Outline each Plasmodium falciparum-infected red blood cell.
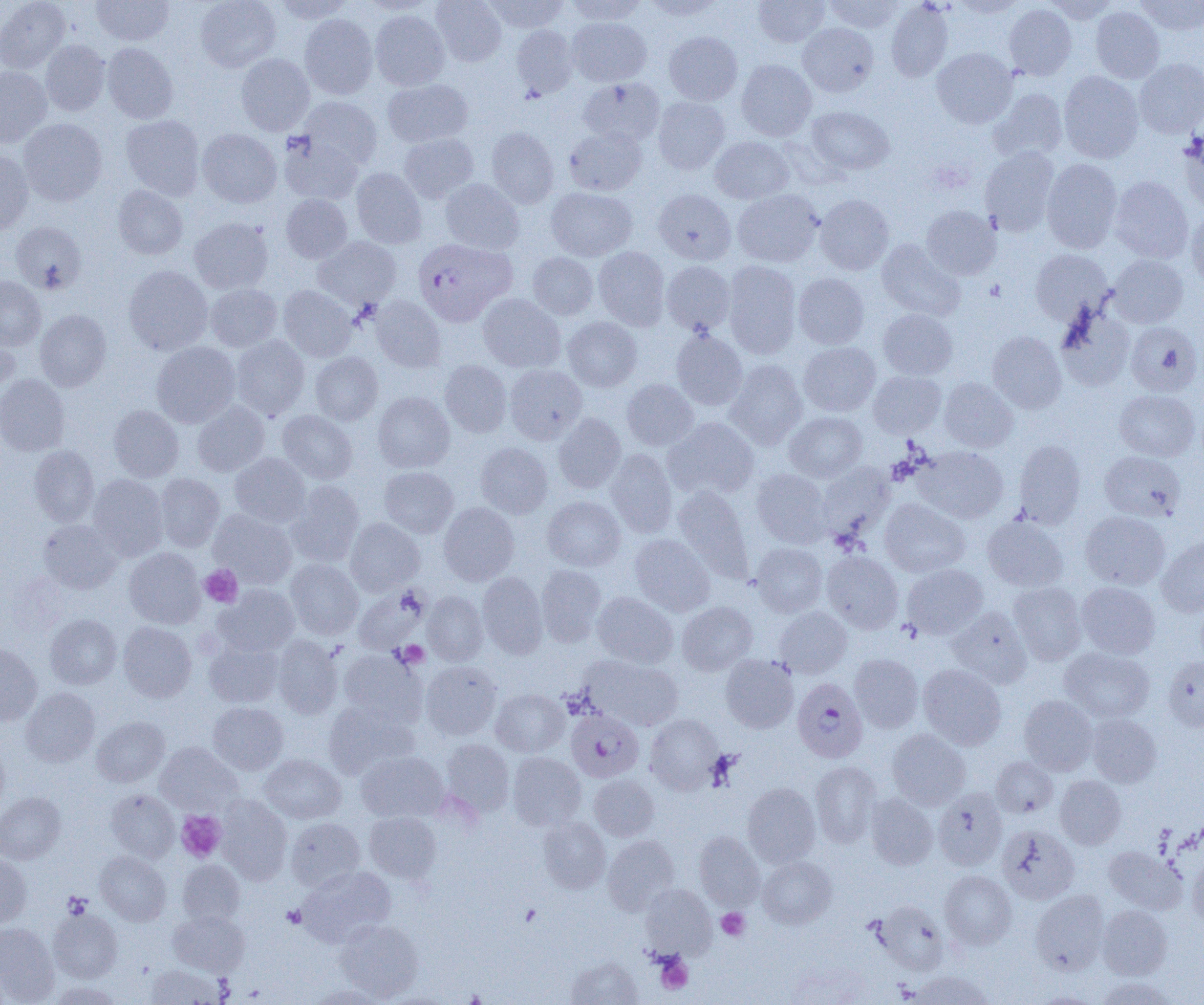

Approximate bounding boxes as [x1, y1, x2, y2] in pixels.
Plasmodium falciparum-infected red blood cells: [413, 238, 515, 326], [792, 678, 868, 762], [566, 709, 644, 782].

Uninfected red blood cell locations: [0, 0, 71, 73], [91, 0, 174, 46], [196, 0, 280, 72], [271, 0, 355, 23], [431, 0, 506, 66], [483, 0, 569, 34], [565, 0, 648, 25], [641, 0, 724, 21], [753, 0, 830, 47], [824, 0, 904, 33], [1042, 0, 1119, 23], [1135, 0, 1204, 35], [886, 1, 953, 82], [1004, 4, 1077, 80], [1091, 6, 1164, 83], [370, 10, 450, 90], [299, 13, 378, 99], [567, 17, 651, 86], [798, 23, 878, 97], [511, 24, 578, 99], [664, 31, 742, 105], [40, 40, 110, 115], [102, 43, 178, 123], [932, 48, 1017, 128], [235, 53, 314, 135], [1135, 58, 1204, 138], [736, 59, 817, 141], [0, 66, 52, 147], [1058, 71, 1144, 163], [578, 77, 665, 146], [382, 79, 473, 147], [989, 88, 1068, 162], [298, 96, 382, 170], [652, 96, 730, 174], [806, 106, 894, 176], [121, 115, 205, 201], [19, 118, 107, 206], [486, 126, 559, 209], [563, 126, 647, 196], [197, 129, 282, 207], [1178, 132, 1204, 211], [399, 134, 478, 203], [279, 135, 363, 205], [710, 136, 794, 204], [980, 147, 1059, 236], [0, 151, 33, 235], [1042, 158, 1122, 253], [351, 167, 427, 248], [1109, 176, 1193, 263], [440, 179, 524, 254], [112, 185, 188, 260], [545, 187, 637, 261], [652, 188, 736, 265], [733, 189, 824, 267], [281, 194, 352, 263], [815, 194, 895, 275], [922, 205, 1000, 280], [1186, 209, 1204, 289], [189, 217, 273, 294], [11, 221, 86, 294], [313, 237, 401, 309], [876, 239, 965, 321], [593, 246, 670, 331], [1030, 250, 1113, 325], [528, 252, 598, 320], [1108, 254, 1188, 327], [661, 261, 735, 335], [723, 261, 802, 359], [123, 265, 212, 355], [793, 273, 869, 349], [0, 276, 46, 350], [205, 283, 282, 351], [278, 285, 356, 361], [478, 294, 565, 372], [371, 296, 446, 372], [1055, 306, 1135, 391], [34, 309, 112, 391], [878, 309, 958, 380], [563, 317, 642, 392], [1126, 321, 1202, 397], [671, 329, 747, 410], [0, 331, 20, 402], [987, 331, 1067, 413], [230, 335, 309, 420], [151, 342, 240, 427], [799, 342, 880, 416], [310, 352, 383, 425], [725, 359, 807, 449], [439, 360, 512, 437], [505, 364, 587, 444], [868, 371, 946, 438], [0, 374, 69, 456], [939, 377, 1017, 452], [622, 379, 698, 451], [1113, 389, 1200, 461], [373, 392, 455, 473], [192, 401, 269, 476], [109, 405, 184, 482], [277, 410, 357, 484], [784, 411, 867, 482], [554, 413, 626, 493], [664, 417, 759, 500], [1014, 440, 1086, 527], [476, 443, 553, 518], [29, 445, 99, 526], [916, 446, 1008, 523], [606, 450, 677, 536], [1099, 450, 1186, 522], [230, 453, 311, 528], [816, 463, 894, 542], [379, 466, 459, 538], [751, 469, 831, 547], [88, 474, 169, 560], [155, 474, 225, 551], [286, 480, 364, 566], [673, 485, 753, 582], [543, 496, 625, 571], [880, 499, 969, 577], [438, 502, 519, 585], [208, 509, 297, 588], [1080, 511, 1170, 590], [982, 514, 1068, 592], [345, 518, 424, 595], [38, 519, 122, 594], [630, 534, 715, 616], [1156, 536, 1204, 617], [751, 543, 827, 616], [124, 547, 206, 628], [821, 551, 903, 633], [285, 559, 363, 639], [902, 564, 987, 639], [536, 565, 606, 646], [477, 572, 547, 658], [1008, 581, 1086, 665], [1076, 582, 1160, 659], [214, 584, 300, 656], [353, 585, 429, 655], [423, 591, 488, 665], [592, 592, 678, 669], [677, 601, 757, 675], [774, 607, 851, 678], [947, 607, 1032, 687], [45, 614, 122, 689], [118, 622, 197, 702], [273, 636, 343, 719], [204, 639, 284, 707], [0, 644, 42, 725], [1060, 647, 1154, 723], [338, 650, 426, 726], [720, 654, 799, 732], [849, 654, 923, 733], [582, 655, 683, 731], [1163, 655, 1204, 733], [420, 661, 501, 740], [919, 664, 1006, 750], [21, 688, 100, 766], [490, 688, 569, 757], [1019, 695, 1099, 775], [323, 700, 418, 779], [208, 702, 288, 774], [645, 714, 724, 794], [1087, 714, 1161, 787], [92, 716, 169, 787], [887, 729, 971, 810], [441, 738, 514, 817], [155, 742, 242, 815], [0, 743, 9, 815], [356, 751, 449, 823], [507, 752, 586, 830], [259, 753, 346, 824], [991, 756, 1057, 818], [810, 761, 881, 848], [589, 775, 659, 841], [1055, 775, 1126, 849], [742, 783, 821, 868], [933, 787, 1008, 870], [106, 789, 179, 862], [0, 792, 66, 864], [866, 793, 938, 870], [215, 795, 292, 884], [365, 812, 441, 883], [285, 817, 365, 891], [538, 817, 610, 893], [997, 825, 1080, 904], [694, 831, 764, 909], [603, 835, 679, 915], [1103, 846, 1186, 913], [94, 851, 171, 925], [0, 852, 32, 927], [1187, 854, 1204, 929], [758, 856, 836, 928], [177, 860, 245, 926], [298, 866, 395, 946], [940, 870, 1016, 949], [641, 884, 717, 958], [1031, 890, 1110, 974], [873, 900, 949, 974], [1097, 905, 1172, 980], [48, 909, 122, 983], [168, 910, 249, 975], [335, 919, 423, 1001], [0, 923, 59, 1003], [565, 956, 642, 1005], [146, 964, 225, 1004], [909, 970, 993, 1004], [1095, 975, 1177, 1005], [49, 981, 120, 1005], [307, 984, 390, 1005]. Platelet locations: [199, 564, 242, 607], [394, 640, 429, 668], [176, 811, 226, 862], [63, 892, 92, 919], [282, 905, 307, 928], [716, 908, 750, 941], [656, 955, 693, 994]. Slide-level diagnosis: Plasmodium falciparum. Light microscopy. Image is 1204×1005 pixels. Single field of view. Captured at 1000x magnification. Thin blood smear.